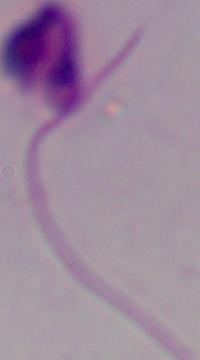

Captured at 1000x magnification. Micrograph. A Leishmania parasite is shown.